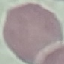

malaria status = uninfected
capture = smartphone camera at the microscope eyepiece
stain = Giemsa
image type = automatically extracted cell patch, resized to 64 × 64 pixels
preparation = thin blood film